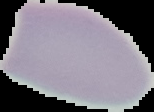 Result: no malaria parasites seen. The area outside the segmented cell region is set to black. Image is 154×112 pixels. From a thin blood film.